Give the preparation type.
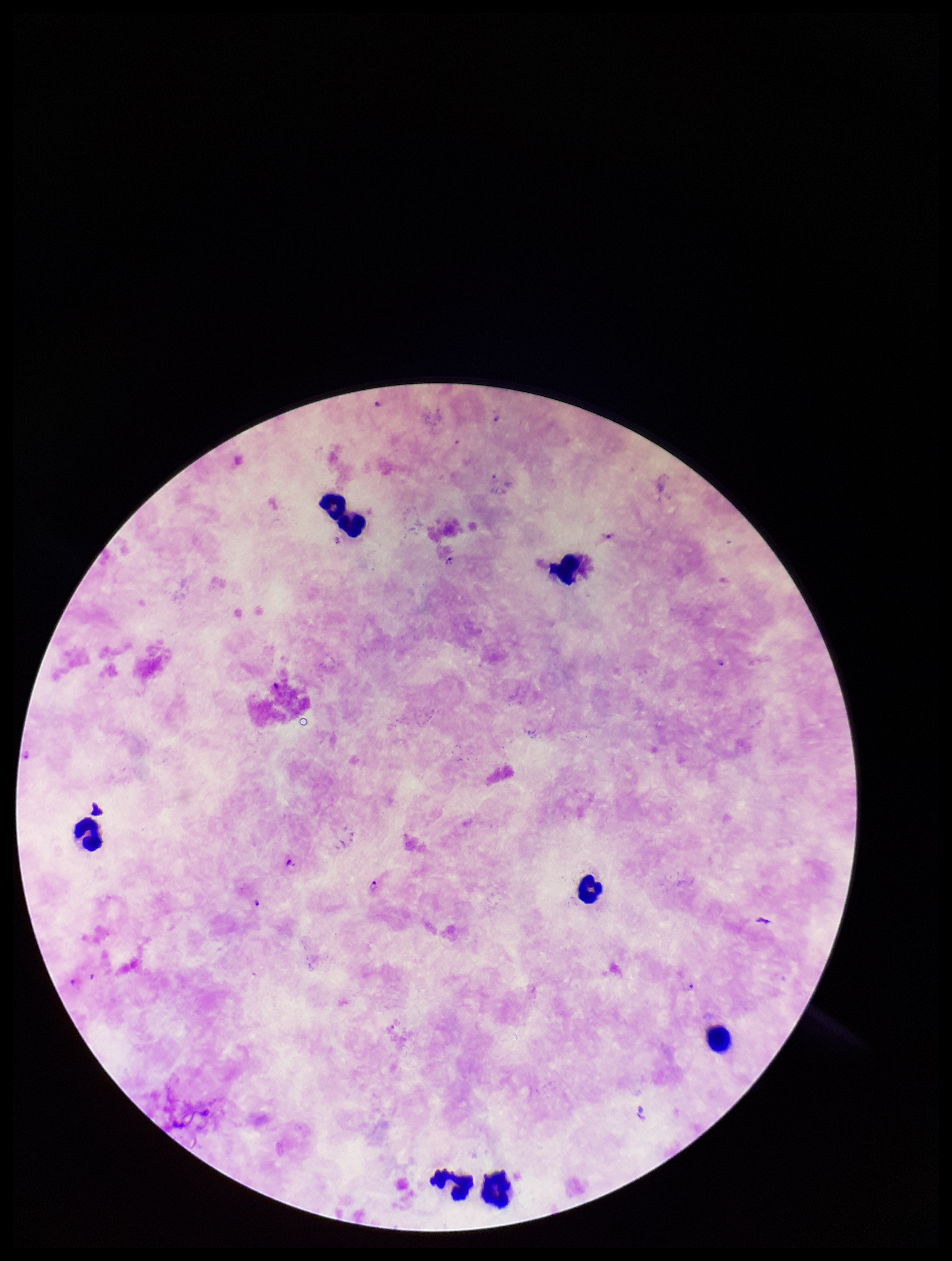

Thick.

Summary:
  - Plasmodium parasites: identified
  - Stain: Giemsa
  - Leukocyte count: 7
  - Species reported for this patient: Plasmodium falciparum
  - Field of view: single
  - Patient malaria status: positive
  - Parasite count: 6
  - Image size: 952×1261 pixels
  - Capture: smartphone photograph through the microscope eyepiece